Give the extent of all Plasmodium malariae-infected red blood cells.
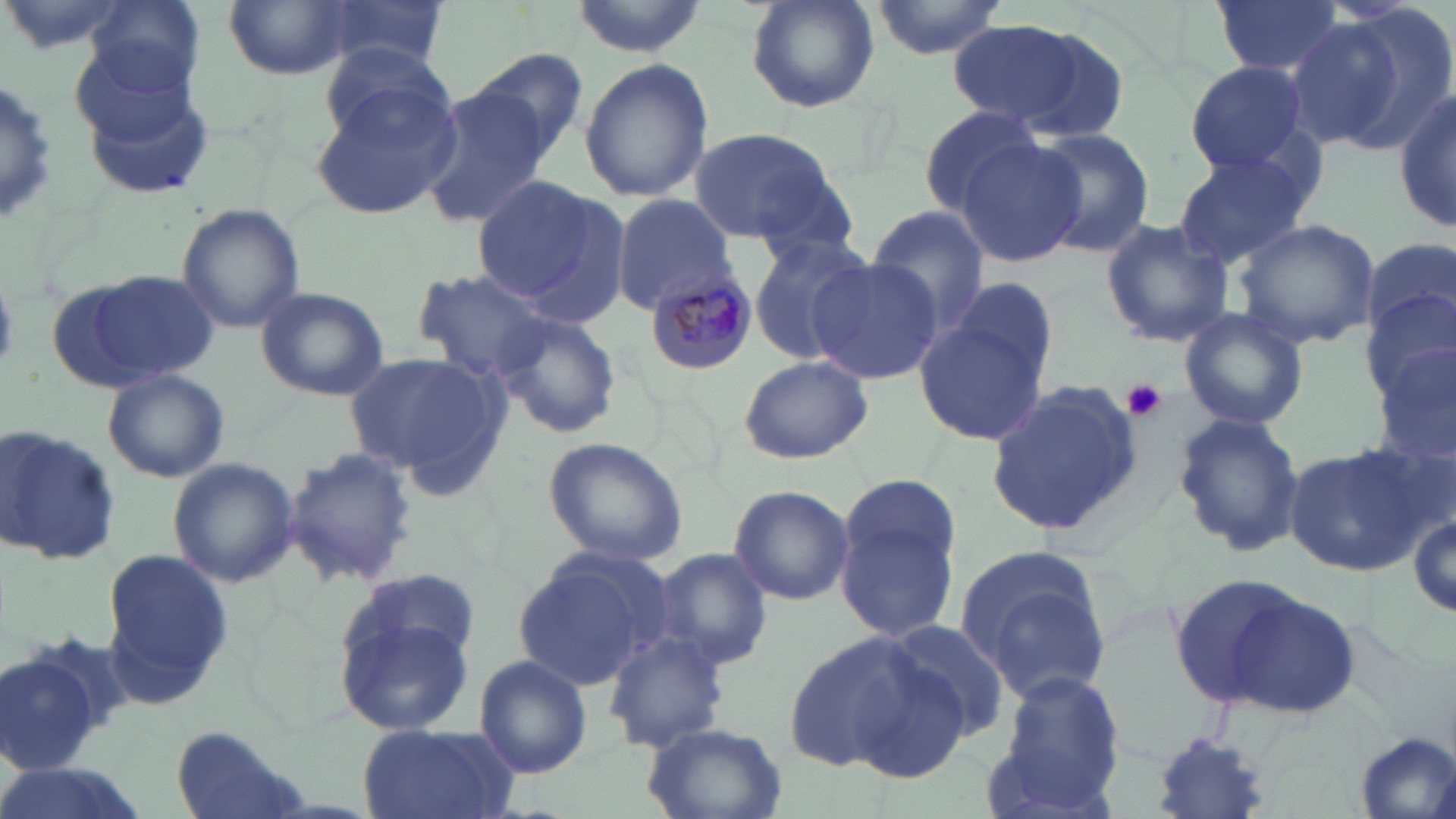

Approximate bounding boxes as (x1, y1, x2, y2) in pixels.
Plasmodium malariae-infected red blood cells: (644, 271, 758, 376).

slide-level diagnosis = Plasmodium malariae
magnification = 1000x
preparation = thin blood smear
field of view = one of a larger specimen
platelet locations = approximate bounding boxes as (x1, y1, x2, y2) in pixels: (1126, 380, 1165, 420)
stain = May-Grünwald-Giemsa
modality = light microscopy
image size = 1456×819 pixels
uninfected red blood cell locations = approximate bounding boxes as (x1, y1, x2, y2) in pixels: (83, 0, 205, 98), (566, 0, 710, 58), (743, 0, 880, 112), (868, 0, 1011, 60), (1212, 0, 1344, 80), (314, 1, 448, 73), (224, 2, 354, 79), (1287, 10, 1448, 153), (945, 20, 1091, 128), (313, 41, 458, 157), (470, 47, 590, 162), (579, 58, 712, 202), (1184, 61, 1310, 176), (76, 77, 219, 205), (0, 78, 62, 227), (311, 78, 462, 221), (418, 87, 547, 226), (1394, 89, 1455, 234), (916, 105, 1049, 216), (688, 126, 839, 245), (1028, 127, 1156, 256), (953, 135, 1085, 269), (1170, 147, 1319, 271), (469, 175, 607, 304), (515, 192, 633, 332), (611, 193, 738, 313), (175, 203, 306, 334), (866, 207, 990, 334), (1235, 218, 1380, 349), (1099, 219, 1235, 348), (747, 233, 877, 366), (1362, 235, 1456, 346), (808, 257, 945, 387), (415, 270, 557, 382), (57, 272, 221, 392), (946, 276, 1059, 391), (254, 284, 389, 401), (1365, 291, 1456, 409), (1177, 308, 1308, 430), (492, 313, 622, 438), (913, 315, 1050, 443), (1374, 347, 1456, 471), (342, 351, 508, 486), (738, 356, 873, 465), (103, 369, 228, 484), (986, 381, 1141, 536), (1171, 412, 1306, 558), (2, 424, 121, 572), (541, 437, 689, 568), (1282, 442, 1436, 575), (285, 445, 415, 587), (166, 456, 299, 587), (727, 484, 852, 606), (834, 488, 962, 645), (1406, 509, 1455, 622), (953, 543, 1115, 701), (100, 544, 234, 712), (511, 547, 670, 690), (653, 547, 774, 673), (1169, 571, 1311, 709), (333, 578, 479, 733), (1221, 592, 1361, 718), (876, 617, 1013, 742), (601, 629, 731, 753), (781, 630, 936, 772), (0, 644, 116, 777), (475, 655, 593, 779), (995, 668, 1126, 798), (642, 722, 789, 819), (356, 723, 519, 819), (171, 728, 315, 819), (1354, 730, 1456, 819), (1149, 734, 1275, 819), (0, 759, 139, 819)